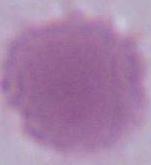

Summary:
  - Magnification: 1000x
  - Identification: red blood cell
  - Modality: micrograph